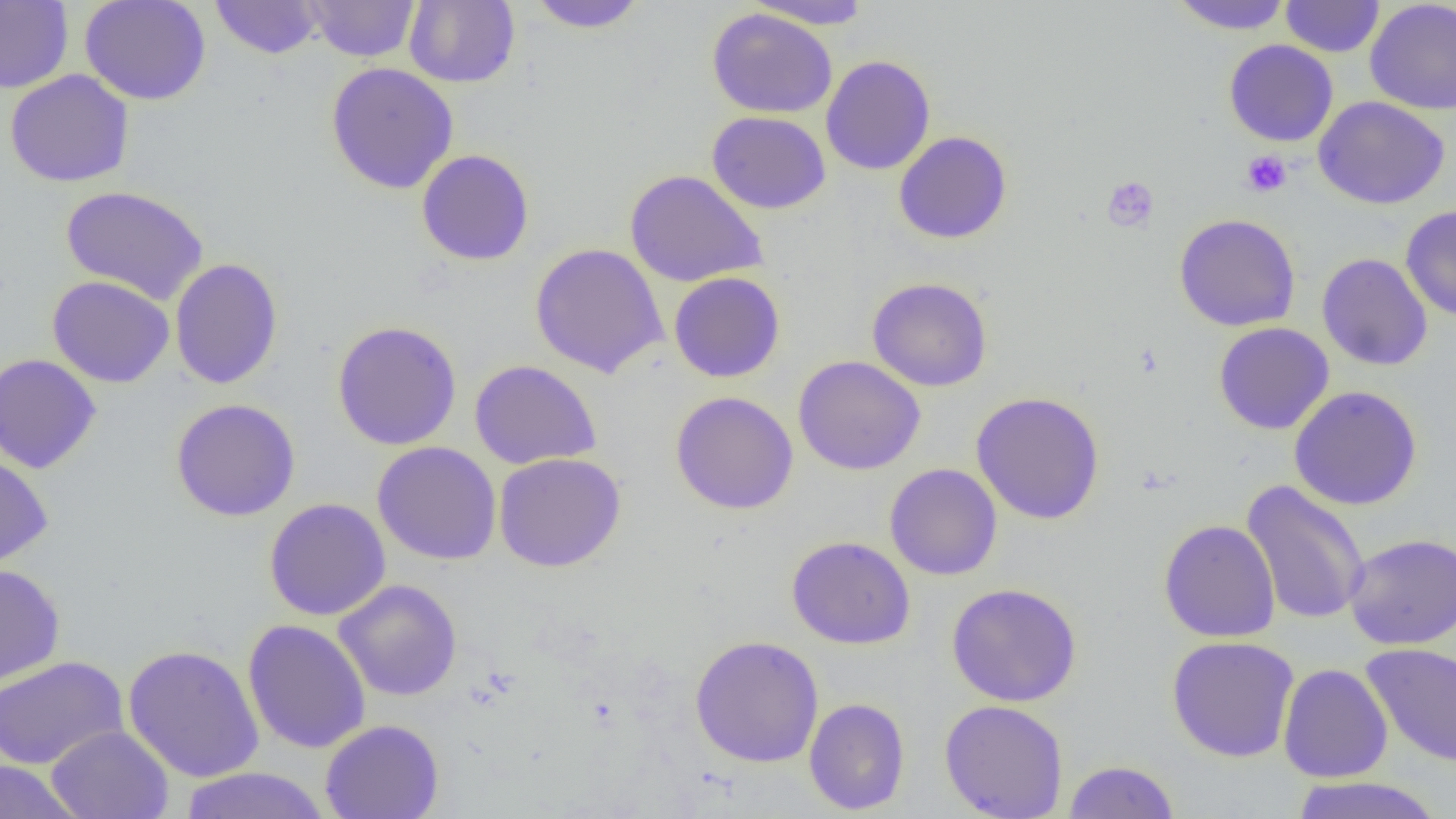

slide-level diagnosis = no evidence of blood parasites
modality = light microscopy
platelet locations = approximate bounding boxes as (x1, y1, x2, y2) in pixels: (1240, 150, 1292, 197), (1102, 176, 1159, 232)
field of view = single
preparation = thin blood film
uninfected red blood cell locations = approximate bounding boxes as (x1, y1, x2, y2) in pixels: (79, 0, 211, 106), (304, 0, 420, 62), (404, 0, 520, 88), (525, 0, 649, 33), (745, 0, 874, 30), (1168, 0, 1295, 35), (1280, 0, 1384, 57), (1364, 0, 1456, 115), (0, 1, 74, 93), (210, 1, 324, 59), (707, 7, 837, 118), (1223, 39, 1339, 146), (821, 55, 935, 175), (325, 62, 459, 194), (4, 69, 134, 188), (1313, 97, 1450, 209), (706, 111, 831, 214), (894, 131, 1012, 245), (417, 149, 534, 266), (624, 169, 768, 287), (60, 185, 209, 305), (1400, 204, 1456, 322), (1173, 213, 1301, 332), (529, 243, 669, 378), (1317, 252, 1433, 371), (169, 258, 284, 390), (668, 271, 785, 383), (47, 275, 175, 388), (867, 277, 993, 392), (331, 319, 462, 450), (1213, 322, 1334, 435), (0, 354, 102, 475), (792, 355, 926, 476), (469, 360, 601, 469), (1289, 385, 1422, 510), (670, 391, 799, 514), (971, 391, 1105, 525), (170, 398, 301, 521), (372, 441, 502, 565), (494, 452, 626, 572), (0, 453, 53, 570), (884, 463, 1002, 580), (1241, 480, 1370, 626), (264, 497, 391, 621), (1158, 519, 1280, 642), (1344, 533, 1456, 650), (787, 535, 916, 649), (0, 563, 66, 686), (334, 579, 463, 701), (946, 582, 1083, 707), (242, 618, 371, 754), (689, 634, 824, 768), (1166, 636, 1300, 762), (121, 643, 265, 783), (1361, 643, 1456, 767), (0, 655, 129, 771), (1278, 663, 1393, 783), (803, 697, 910, 815), (939, 699, 1069, 819), (320, 719, 444, 819), (45, 725, 174, 819), (1062, 759, 1181, 819), (0, 761, 84, 819), (178, 767, 332, 818), (1290, 775, 1445, 819)
image size = 1456×819 pixels
magnification = 1000x